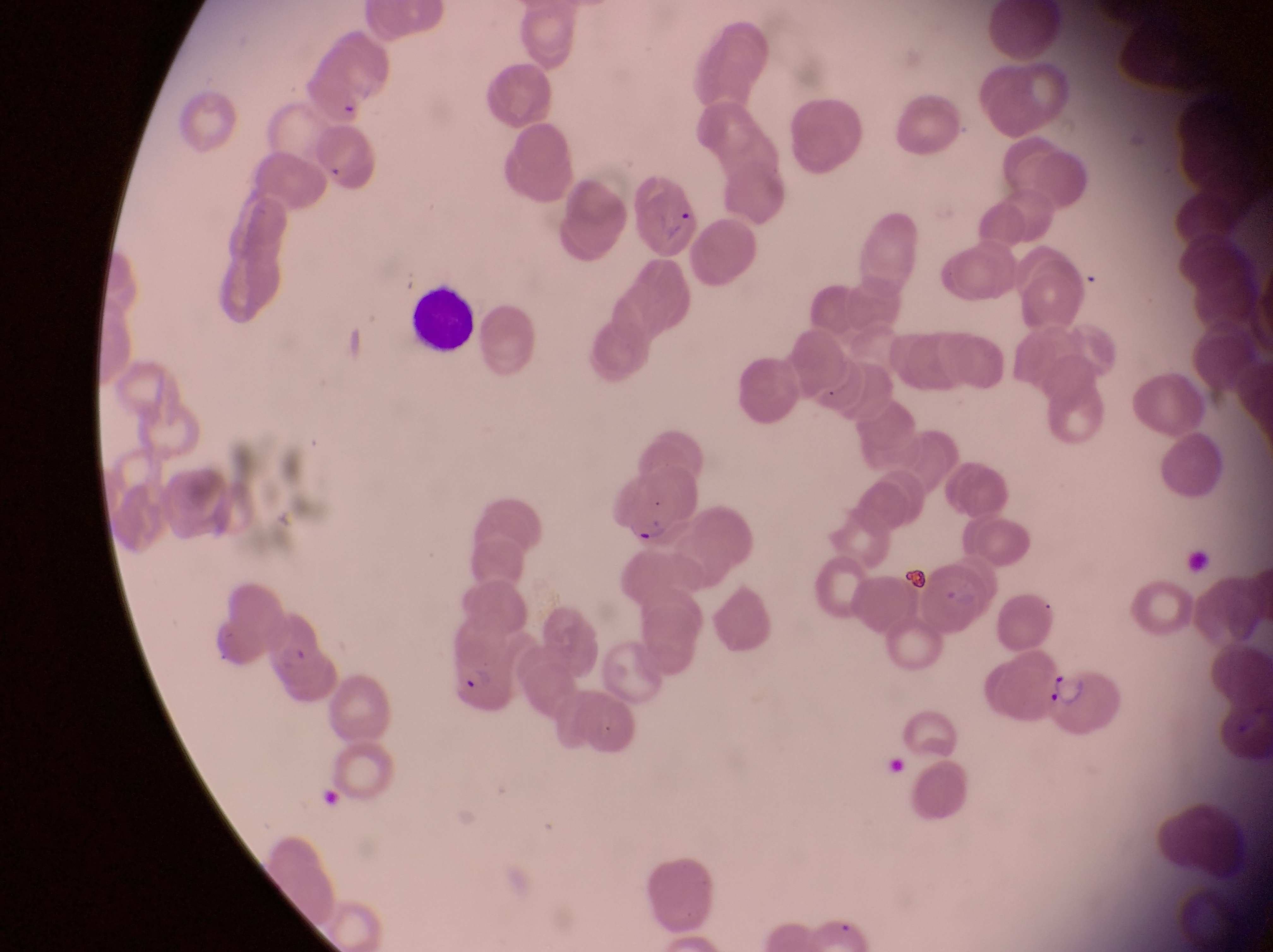
parasitised red blood cell locations = approximate bounding boxes as {left, top, right, bottom} in pixels: {633, 174, 698, 255}, {607, 480, 695, 548}, {254, 611, 321, 674}, {442, 644, 520, 718}, {1049, 670, 1132, 745}
capture = smartphone photograph through the eyepiece of an Olympus CX-23 microscope
image size = 1273×952 pixels
preparation = thin blood smear
leukocyte locations = approximate bounding boxes as {left, top, right, bottom} in pixels: {408, 290, 481, 351}
country = Uganda
magnification = 1000x
field of view = single